Assess the morphology of the red blood cells.
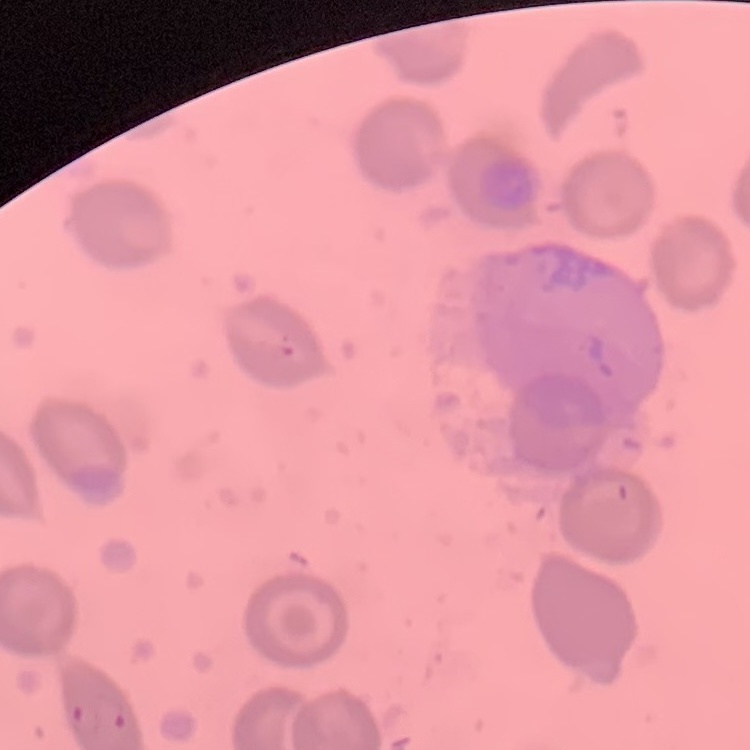

No rouleaux formation.

preparation = thin blood smear
image type = one tile cut from a larger photomicrograph
stain = Field's or Giemsa